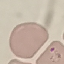

Malaria status: parasitized. Acquired by smartphone through the microscope eyepiece. Thin smear of blood. Giemsa-stained preparation. Cell patch, automatically extracted from a larger field of view and resized to 64 × 64 pixels.